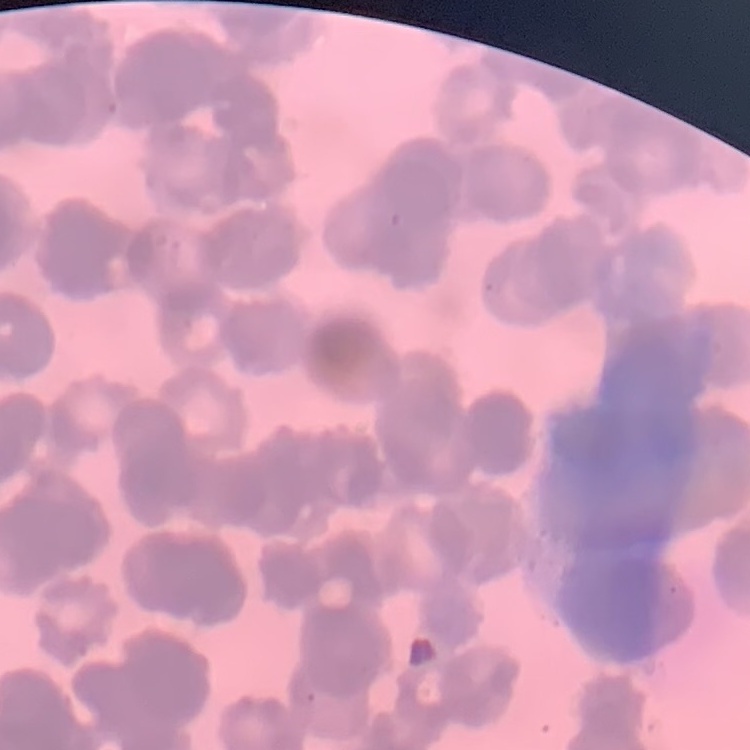
The erythrocytes exhibit rouleaux formation. Thin blood smear. One tile cut from a larger photomicrograph. Field's or Giemsa stain.